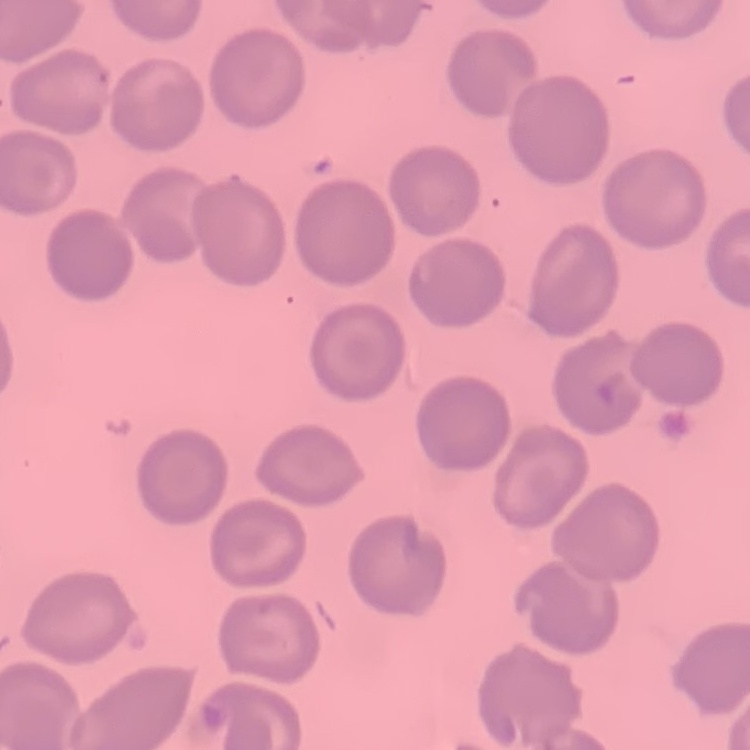
red_blood_cell_morphology: no rouleaux formation
preparation: thin blood film
stain: Field's or Giemsa
image_type: square crop of a larger photomicrograph